Identify the parasite.
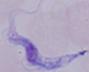

A trypanosome.

Summary:
  - Magnification: 1000x
  - Modality: photomicrograph